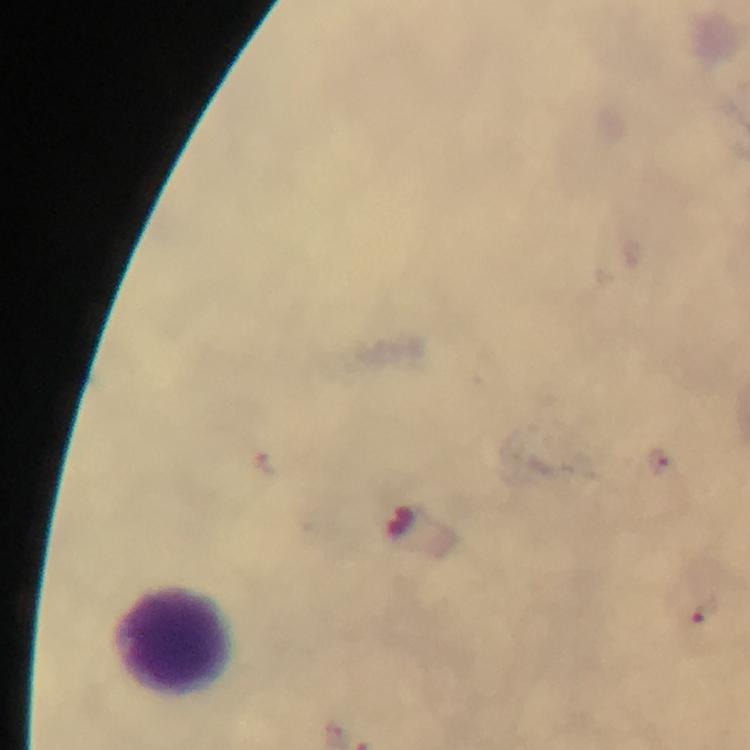

{
  "capture": "smartphone camera through the microscope",
  "plasmodium_parasite_locations": "approximate object centers, in pixels from the top-left corner: (x=660, y=464), (x=265, y=465), (x=708, y=612)",
  "cropped_from": "one field of view",
  "image_size": "750×750 pixels",
  "magnification": "100x",
  "preparation": "thick smear",
  "leukocyte_locations": "approximate object centers, in pixels from the top-left corner: (x=177, y=641)",
  "stain": "Giemsa",
  "context": "from a malaria diagnostic workup",
  "immersion_oil": "applied"
}